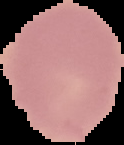

Summary:
  - Image type: cell region segmented out of the field of view; surrounding area masked to black
  - Image size: 124×145 pixels
  - Malaria status: uninfected
  - Preparation: thin blood smear